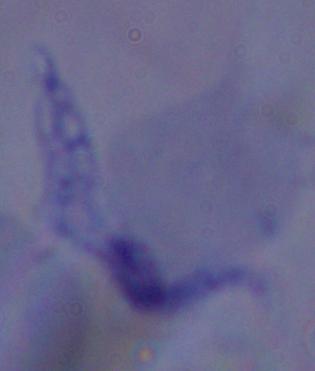 1000x magnification. Photomicrograph. A trypanosome is shown.